Point out every Plasmodium parasite and every leukocyte.
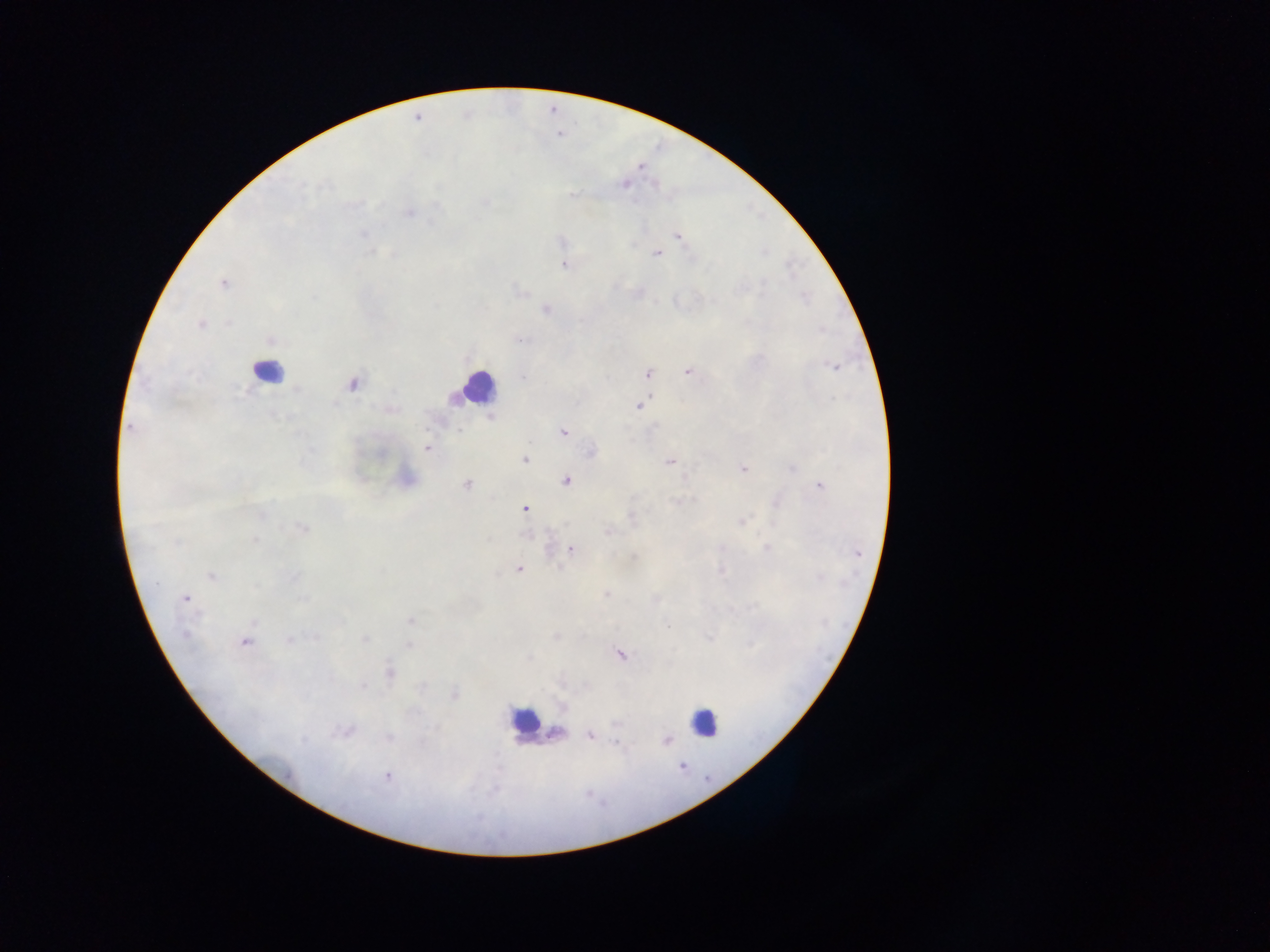

Approximate centers as [x, y] in pixels.
Plasmodium parasites: [417, 118], [624, 184], [410, 213], [678, 235], [657, 253], [564, 264], [223, 283], [520, 292], [546, 309], [201, 323], [271, 340], [519, 340], [836, 367], [688, 371], [647, 374], [352, 384], [639, 406], [489, 417], [130, 428], [563, 431], [427, 448], [591, 451], [525, 459], [669, 461], [742, 469], [406, 477], [567, 480], [467, 484], [820, 485], [679, 501], [525, 509], [741, 521], [302, 528], [608, 532], [767, 546], [571, 549], [518, 568], [212, 575], [606, 594], [185, 598], [410, 620], [556, 636], [291, 639], [709, 639], [245, 641], [408, 645], [620, 655], [389, 673], [454, 694], [345, 730], [589, 734], [665, 741], [386, 775].
Leukocytes: [265, 371], [477, 387], [525, 721], [703, 722], [557, 733].

Summary:
  - Preparation: thick blood smear
  - Capture: mobile-phone photograph through a microscope
  - Field of view: single
  - Country: Ghana
  - Image size: 1270×952 pixels